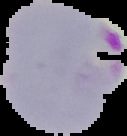
preparation = thin blood film
image type = segmented cell region on a black background
image size = 127×136 pixels
malaria status = parasitized